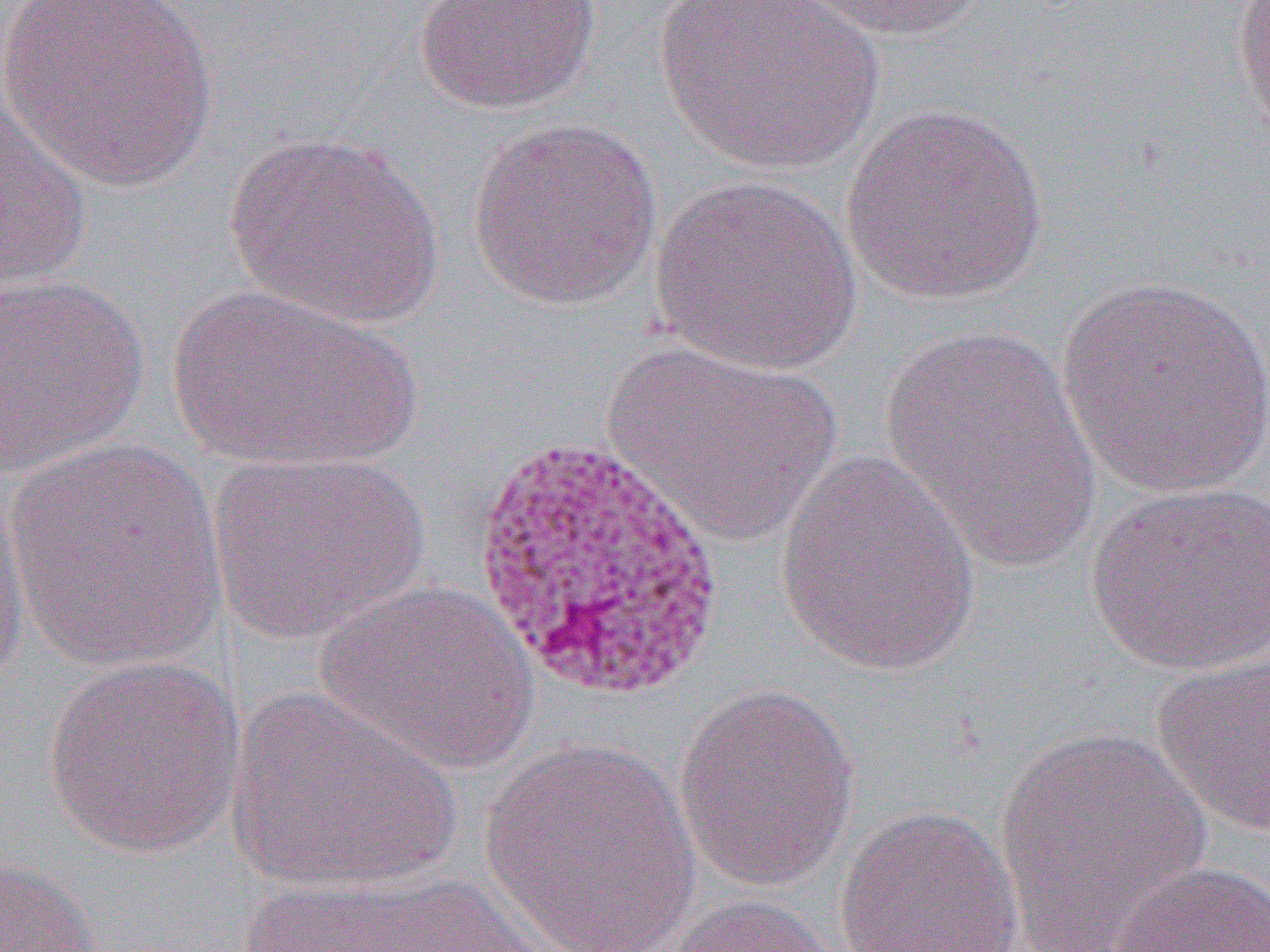
Summary:
  - Coordinate format: approximate bounding boxes as [x1, y1, x2, y2] in pixels
  - Uninfected red blood cell locations: [3, 0, 220, 190], [412, 0, 601, 114], [791, 0, 985, 43], [1232, 0, 1270, 146], [653, 1, 887, 176], [0, 97, 94, 293], [840, 101, 1049, 307], [466, 117, 664, 311], [224, 131, 444, 327], [648, 176, 863, 376], [0, 272, 149, 479], [1055, 273, 1270, 504], [164, 285, 425, 475], [878, 325, 1101, 575], [600, 340, 842, 546], [4, 437, 229, 674], [208, 450, 429, 642], [776, 451, 985, 676], [0, 467, 32, 689], [1085, 482, 1270, 677], [316, 580, 538, 776], [1151, 648, 1270, 839], [41, 655, 246, 859], [672, 683, 861, 891], [225, 685, 462, 894], [992, 726, 1213, 947], [479, 738, 701, 948], [834, 805, 1025, 952], [0, 854, 102, 951], [1108, 859, 1270, 952], [240, 872, 548, 952], [660, 892, 850, 952]
  - Slide-level diagnosis: Plasmodium vivax
  - Magnification: 1000x
  - Preparation: thin blood smear
  - Modality: optical microscopy
  - Image size: 1270×952 pixels
  - Field of view: one of a larger specimen